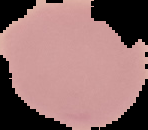
From a thin blood film. The area outside the segmented cell region is set to black. Image is 148×130 pixels. Malaria status: uninfected.